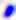
Summary:
  - Magnification: 400x
  - Modality: micrograph
  - Identification: Toxoplasma gondii